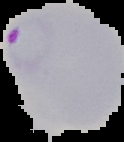
preparation: thin blood film
malaria_status: parasitized
image_type: cell region segmented out of the field of view; surrounding area masked to black
image_size: 124×142 pixels